Describe the morphology of the erythrocytes.
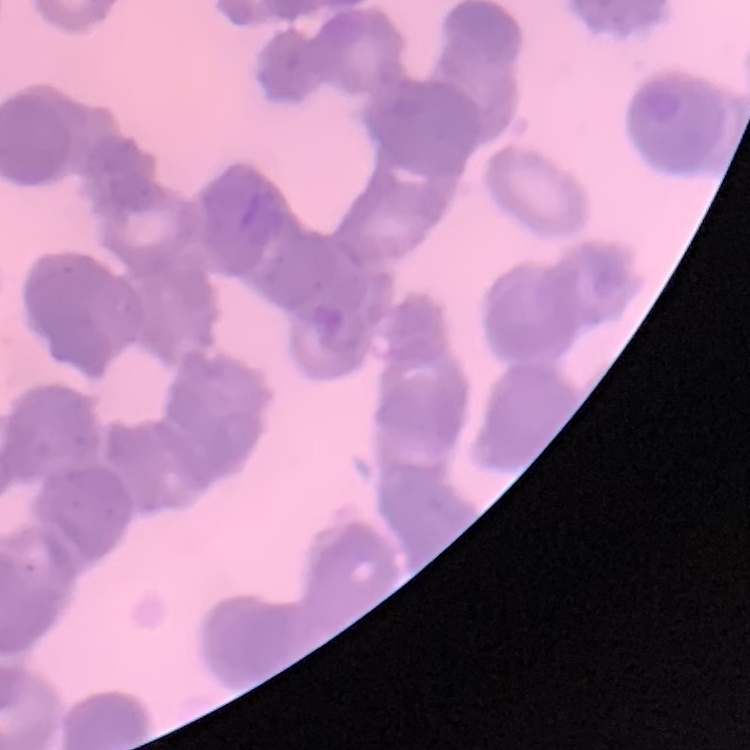

Rouleaux formation.

stain = Field's or Giemsa
image type = one tile cut from a larger photomicrograph
preparation = thin blood film